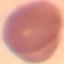
Summary:
  - Result: no malaria parasites detected
  - Stain: Giemsa
  - Capture: smartphone through the microscope eyepiece
  - Preparation: thin blood smear
  - Image type: automatically extracted cell patch, resized to 64 × 64 pixels